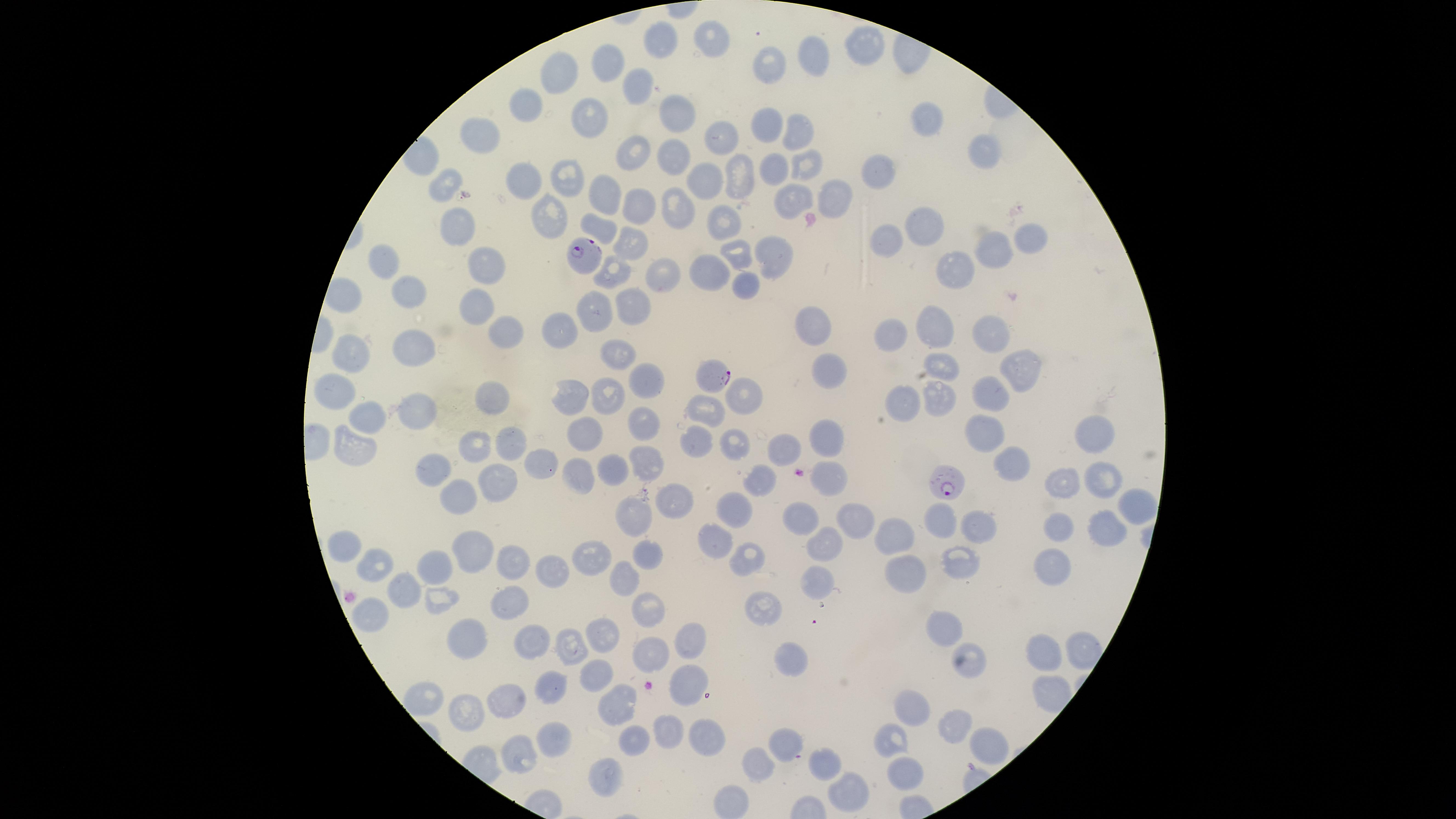
Approximate marker points, in pixels from the top-left corner.
Summary:
  - Uninfected RBCs: (x=712, y=38), (x=663, y=39), (x=858, y=43), (x=816, y=56), (x=609, y=60), (x=773, y=64), (x=558, y=74), (x=641, y=82), (x=532, y=103), (x=677, y=110), (x=591, y=114), (x=927, y=116), (x=766, y=124), (x=717, y=130), (x=479, y=134), (x=796, y=136), (x=636, y=150), (x=680, y=152), (x=984, y=152), (x=808, y=162), (x=778, y=165), (x=878, y=171), (x=569, y=176), (x=741, y=176), (x=706, y=177), (x=524, y=179), (x=446, y=185), (x=791, y=196), (x=833, y=198), (x=640, y=205), (x=674, y=210), (x=550, y=213), (x=717, y=221), (x=926, y=225), (x=456, y=228), (x=1035, y=235), (x=883, y=238), (x=633, y=242), (x=989, y=245), (x=734, y=252), (x=773, y=255), (x=480, y=264), (x=386, y=266), (x=962, y=268), (x=709, y=270), (x=612, y=273), (x=658, y=279), (x=746, y=282), (x=410, y=291), (x=631, y=303), (x=476, y=306), (x=602, y=311), (x=936, y=323), (x=812, y=326), (x=559, y=331), (x=891, y=335), (x=511, y=336), (x=990, y=336), (x=418, y=347), (x=612, y=353), (x=355, y=356), (x=938, y=362), (x=831, y=368), (x=1019, y=369), (x=649, y=380), (x=338, y=391), (x=992, y=392), (x=576, y=393), (x=609, y=395), (x=744, y=396), (x=935, y=398), (x=493, y=400), (x=909, y=401), (x=704, y=405), (x=417, y=413), (x=370, y=419), (x=643, y=425), (x=989, y=433), (x=1093, y=434), (x=700, y=437), (x=585, y=438), (x=825, y=438), (x=736, y=441), (x=514, y=443), (x=782, y=448), (x=349, y=450), (x=471, y=455), (x=647, y=459), (x=1014, y=463), (x=437, y=469), (x=612, y=469), (x=579, y=473), (x=831, y=473), (x=1062, y=476), (x=1105, y=477), (x=498, y=478), (x=760, y=479), (x=457, y=496), (x=676, y=502), (x=1131, y=502), (x=735, y=507), (x=636, y=515), (x=855, y=516), (x=795, y=519), (x=938, y=520), (x=978, y=523), (x=1058, y=524), (x=1101, y=525), (x=718, y=534), (x=896, y=539), (x=347, y=541), (x=647, y=550), (x=469, y=551), (x=821, y=552), (x=955, y=555), (x=591, y=558), (x=1051, y=559), (x=511, y=561), (x=381, y=563), (x=555, y=566), (x=435, y=570), (x=907, y=575), (x=628, y=576), (x=405, y=585), (x=811, y=586), (x=511, y=599), (x=761, y=606), (x=648, y=607), (x=370, y=612), (x=939, y=626), (x=600, y=632), (x=537, y=637), (x=691, y=640), (x=575, y=644), (x=469, y=647), (x=651, y=650), (x=1048, y=652), (x=789, y=663), (x=973, y=663), (x=597, y=671), (x=550, y=683), (x=687, y=685), (x=424, y=693), (x=513, y=701), (x=624, y=702), (x=915, y=707), (x=470, y=711), (x=953, y=719), (x=673, y=729), (x=703, y=735), (x=553, y=737), (x=893, y=737), (x=634, y=738), (x=788, y=741), (x=988, y=746), (x=516, y=755), (x=828, y=769), (x=904, y=770), (x=609, y=772), (x=749, y=772), (x=849, y=791)
  - Parasitized RBCs: (x=580, y=251), (x=710, y=376), (x=944, y=483)
  - Species: Plasmodium falciparum
  - Preparation: thin smear of blood
  - Capture: smartphone photograph through the microscope eyepiece
  - Field of view: single
  - Stain: Giemsa
  - Visible region: circular
  - Image size: 1456×819 pixels
  - Presence: malaria parasites identified